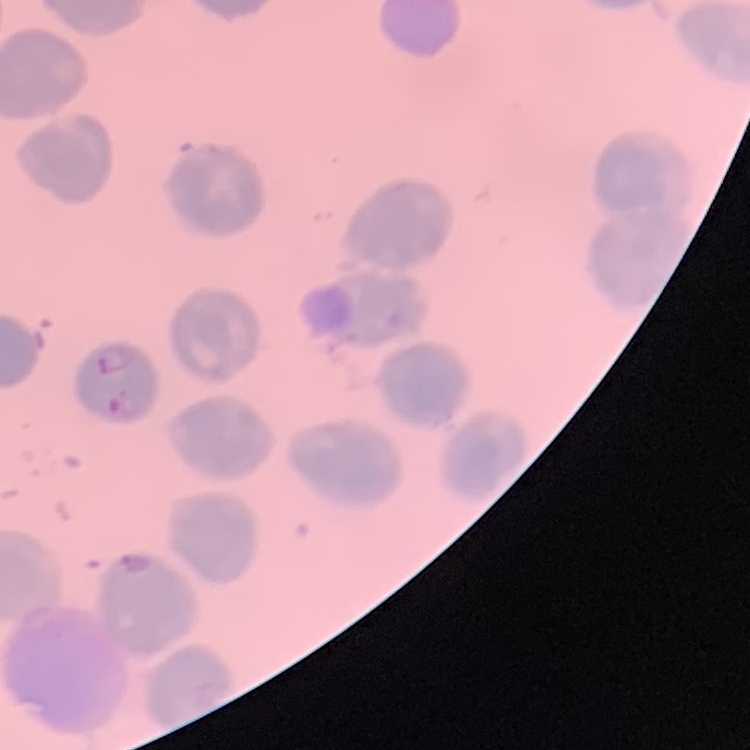

Summary:
  - Red blood cell morphology: no rouleaux formation
  - Image type: one tile cut from a larger photomicrograph
  - Stain: Field's or Giemsa
  - Preparation: thin blood film